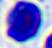 400x magnification. A white blood cell is seen. Micrograph.